Outline every malaria parasite.
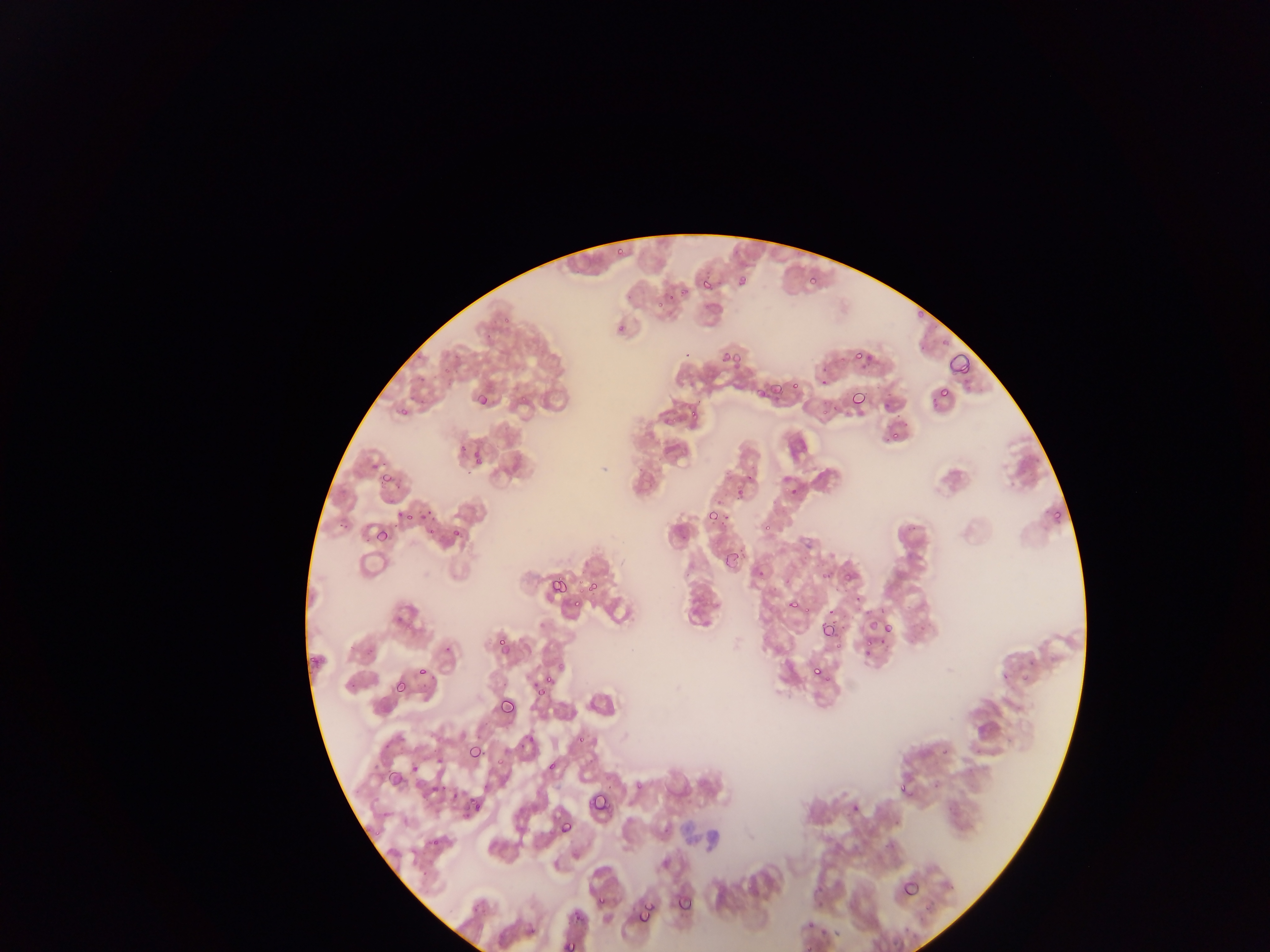

Approximate bounding boxes as (left, top, right, bottom) in pixels.
Malaria parasites: (617, 248, 625, 256), (700, 274, 713, 290), (806, 277, 818, 285), (615, 320, 627, 335), (854, 347, 863, 358), (867, 351, 875, 365), (718, 352, 731, 362), (731, 353, 740, 361), (950, 353, 970, 375), (771, 382, 782, 395), (934, 388, 950, 398), (475, 392, 486, 404), (852, 395, 866, 407), (400, 405, 416, 415), (888, 431, 904, 440), (470, 445, 481, 465), (381, 475, 393, 484), (403, 507, 427, 524), (705, 510, 719, 522), (450, 527, 466, 539), (374, 531, 391, 545), (725, 550, 739, 568), (842, 569, 855, 583), (552, 580, 566, 590), (584, 582, 600, 594), (571, 596, 584, 609), (783, 596, 802, 615), (867, 618, 879, 632), (881, 619, 902, 635), (822, 624, 835, 638), (496, 638, 506, 652), (864, 638, 880, 658), (813, 666, 822, 679), (415, 670, 427, 676), (532, 674, 553, 695), (393, 683, 405, 693), (499, 702, 515, 718), (518, 733, 536, 749), (575, 733, 591, 746), (466, 735, 482, 763), (496, 750, 509, 767), (546, 760, 561, 774), (407, 761, 419, 772), (386, 770, 400, 790), (427, 780, 447, 794), (898, 783, 908, 794), (590, 794, 606, 812), (462, 798, 483, 816), (560, 821, 571, 837), (899, 878, 923, 899), (676, 891, 690, 911), (598, 894, 611, 906), (470, 901, 490, 916), (637, 901, 653, 923), (571, 909, 583, 926), (559, 939, 581, 952).

Image is 1270×952 pixels. Mobile-phone photograph taken through the microscope. Collected in Ghana. One field of view. Thin blood smear.